Point out each leukocyte.
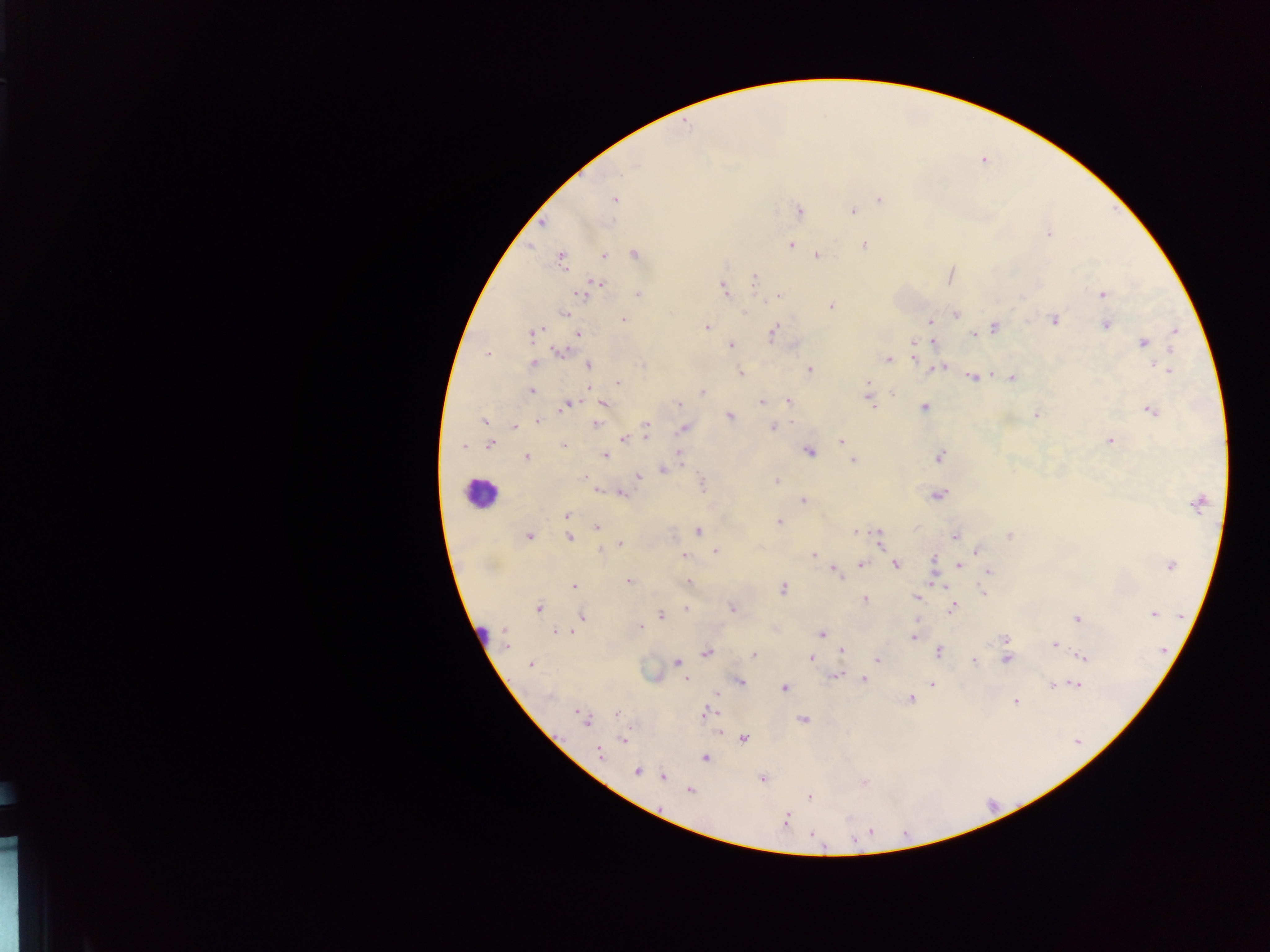
Approximate centers as [x, y] in pixels.
Leukocytes: [480, 493].

Summary:
  - Malaria parasite locations: [635, 165], [613, 200], [879, 200], [799, 211], [852, 211], [541, 223], [1048, 233], [790, 245], [864, 245], [633, 254], [603, 255], [816, 256], [561, 257], [949, 275], [754, 278], [596, 284], [724, 289], [583, 293], [638, 294], [1102, 295], [778, 296], [830, 305], [745, 311], [565, 313], [954, 313], [623, 320], [1053, 320], [930, 321], [1106, 324], [707, 326], [994, 327], [1174, 332], [773, 333], [533, 334], [576, 334], [971, 334], [932, 342], [1143, 343], [731, 344], [914, 344], [558, 350], [487, 353], [888, 359], [915, 359], [533, 363], [588, 365], [943, 367], [935, 368], [809, 369], [1169, 371], [741, 374], [990, 376], [1012, 376], [971, 377], [618, 383], [529, 390], [701, 392], [893, 393], [868, 397], [762, 401], [788, 401], [602, 403], [566, 404], [678, 404], [924, 407], [1150, 410], [1036, 415], [730, 416], [484, 421], [538, 421], [596, 424], [513, 426], [645, 426], [772, 426], [683, 428], [646, 436], [624, 438], [1109, 440], [840, 441], [489, 444], [563, 445], [463, 447], [809, 451], [679, 453], [604, 455], [526, 457], [939, 457], [853, 460], [663, 469], [638, 476], [584, 478], [776, 481], [702, 483], [598, 489], [620, 492], [937, 495], [803, 500], [1198, 501], [566, 515], [778, 521], [597, 526], [698, 532], [855, 532], [1009, 535], [527, 536], [954, 536], [568, 537], [879, 540], [620, 543], [600, 550], [715, 551], [976, 552], [814, 554], [684, 555], [933, 559], [895, 564], [860, 565], [958, 566], [1170, 566], [833, 570], [988, 571], [838, 578], [629, 581], [688, 582], [933, 582], [574, 586], [783, 588], [983, 592], [914, 597], [864, 599], [538, 607], [685, 608], [732, 608], [952, 608], [1153, 613], [660, 614], [583, 616], [1077, 619], [639, 626], [775, 628], [558, 630], [821, 633], [913, 636], [1004, 639], [505, 640], [1054, 645], [841, 650], [939, 651], [706, 652], [754, 654], [1081, 656], [811, 658], [877, 659], [1006, 659], [972, 661], [676, 663], [531, 664], [835, 675], [685, 678], [862, 678], [739, 681], [932, 684], [1052, 684], [1075, 684], [783, 687], [717, 694], [910, 698], [1016, 701], [617, 713], [705, 713], [583, 717], [804, 719], [716, 731], [623, 738], [743, 739], [600, 753], [705, 757], [636, 771], [663, 777], [762, 778], [863, 782], [689, 791], [809, 796], [785, 820]
  - Preparation: thick blood film
  - Capture: mobile-phone photograph through a microscope
  - Image size: 1270×952 pixels
  - Country: Ghana
  - Field of view: single